Locate and identify every blood parasite.
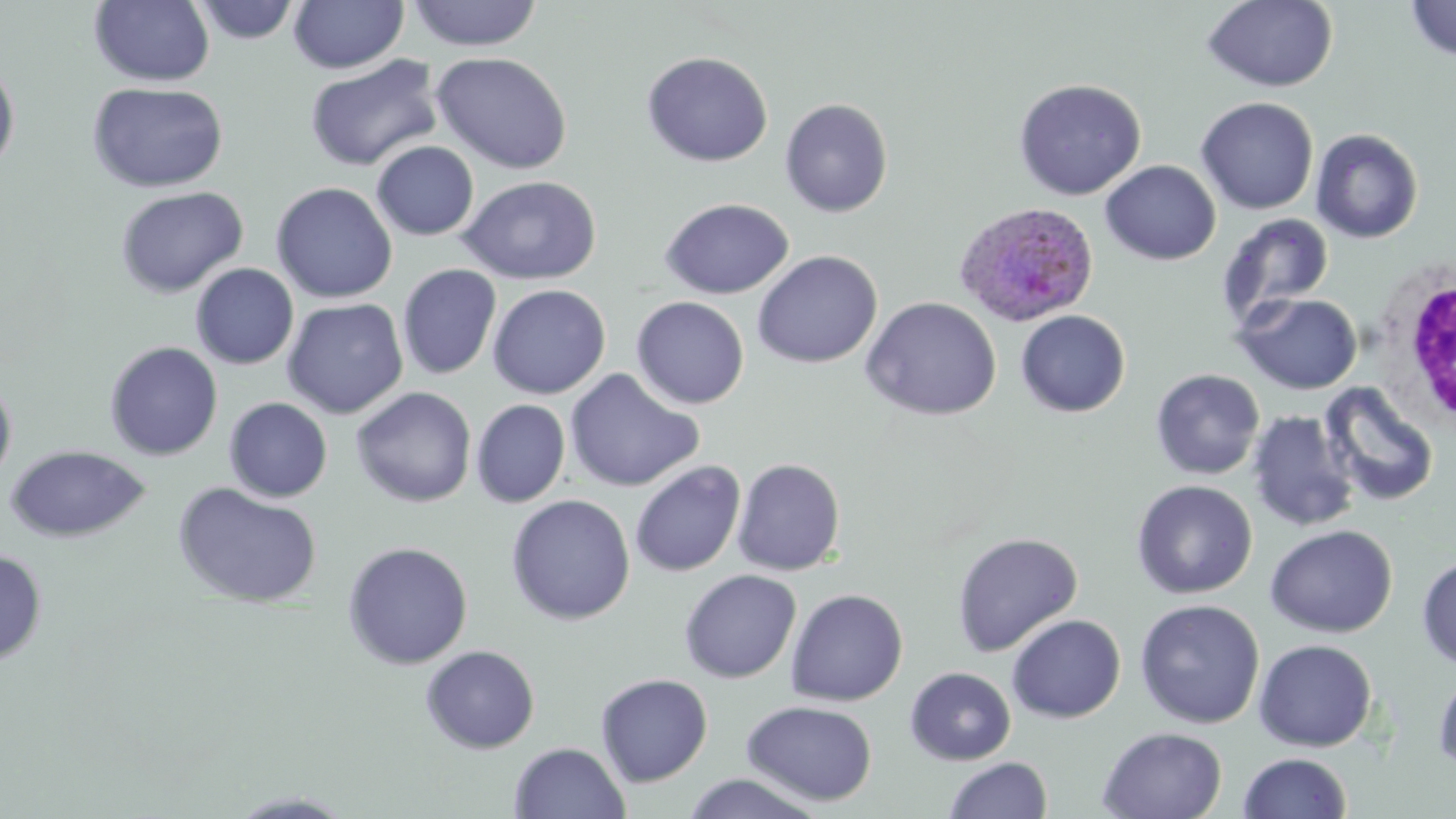
Approximate bounding boxes as [x1, y1, x2, y2] in pixels.
Plasmodium ovale-infected red blood cells: [953, 202, 1100, 327].
No Plasmodium falciparum, Plasmodium malariae, Plasmodium vivax, Babesia divergens, or Trypanosoma brucei observed.

Summary:
  - White blood cell locations: [1375, 260, 1456, 433]
  - Uninfected red blood cell locations: [190, 0, 302, 44], [288, 0, 409, 73], [407, 0, 542, 51], [1202, 0, 1339, 93], [1404, 0, 1456, 62], [89, 1, 215, 86], [432, 51, 573, 175], [641, 51, 774, 167], [305, 55, 444, 172], [0, 58, 20, 176], [1013, 78, 1146, 199], [88, 81, 229, 193], [1195, 97, 1319, 215], [779, 98, 893, 217], [1310, 128, 1424, 243], [371, 141, 479, 241], [1100, 159, 1222, 265], [457, 175, 601, 285], [270, 181, 397, 303], [114, 186, 249, 299], [659, 197, 794, 299], [1216, 213, 1334, 330], [752, 250, 883, 369], [191, 263, 299, 369], [398, 264, 502, 379], [487, 284, 611, 399], [1234, 292, 1363, 395], [631, 296, 749, 409], [860, 296, 1002, 421], [282, 298, 408, 418], [1015, 310, 1130, 417], [104, 341, 223, 461], [565, 368, 705, 492], [1150, 368, 1265, 480], [0, 376, 17, 488], [1319, 382, 1440, 508], [350, 386, 477, 508], [224, 397, 332, 503], [471, 399, 571, 507], [1246, 410, 1360, 533], [4, 445, 152, 542], [732, 458, 846, 576], [630, 460, 746, 577], [1131, 479, 1258, 599], [173, 482, 323, 608], [506, 494, 635, 625], [1265, 524, 1398, 638], [951, 532, 1083, 656], [342, 541, 473, 670], [0, 549, 47, 666], [1416, 555, 1456, 671], [679, 569, 801, 683], [786, 588, 908, 706], [1135, 599, 1265, 729], [1007, 614, 1126, 723], [1253, 639, 1378, 752], [420, 644, 540, 754], [906, 667, 1016, 765], [1432, 669, 1456, 778], [595, 673, 713, 787], [742, 700, 878, 806], [1097, 726, 1228, 819], [509, 742, 630, 819], [1237, 752, 1352, 819], [943, 756, 1053, 819], [680, 773, 827, 818], [227, 790, 357, 818]
  - Slide-level diagnosis: Plasmodium ovale
  - Field of view: single
  - Preparation: thin blood film
  - Modality: light microscopy
  - Stain: May-Grünwald-Giemsa
  - Magnification: 1000x
  - Image size: 1456×819 pixels